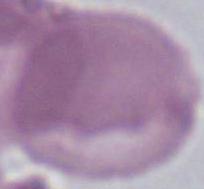

identification = red blood cell
magnification = 1000x
modality = micrograph